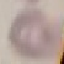
Summary:
  - Malaria status: uninfected
  - Preparation: thin blood film
  - Capture: smartphone camera at the microscope eyepiece
  - Image type: automatically extracted cell patch, resized to 64 × 64 pixels
  - Stain: Giemsa